Locate every Plasmodium falciparum parasite and identify its life-cycle stage.
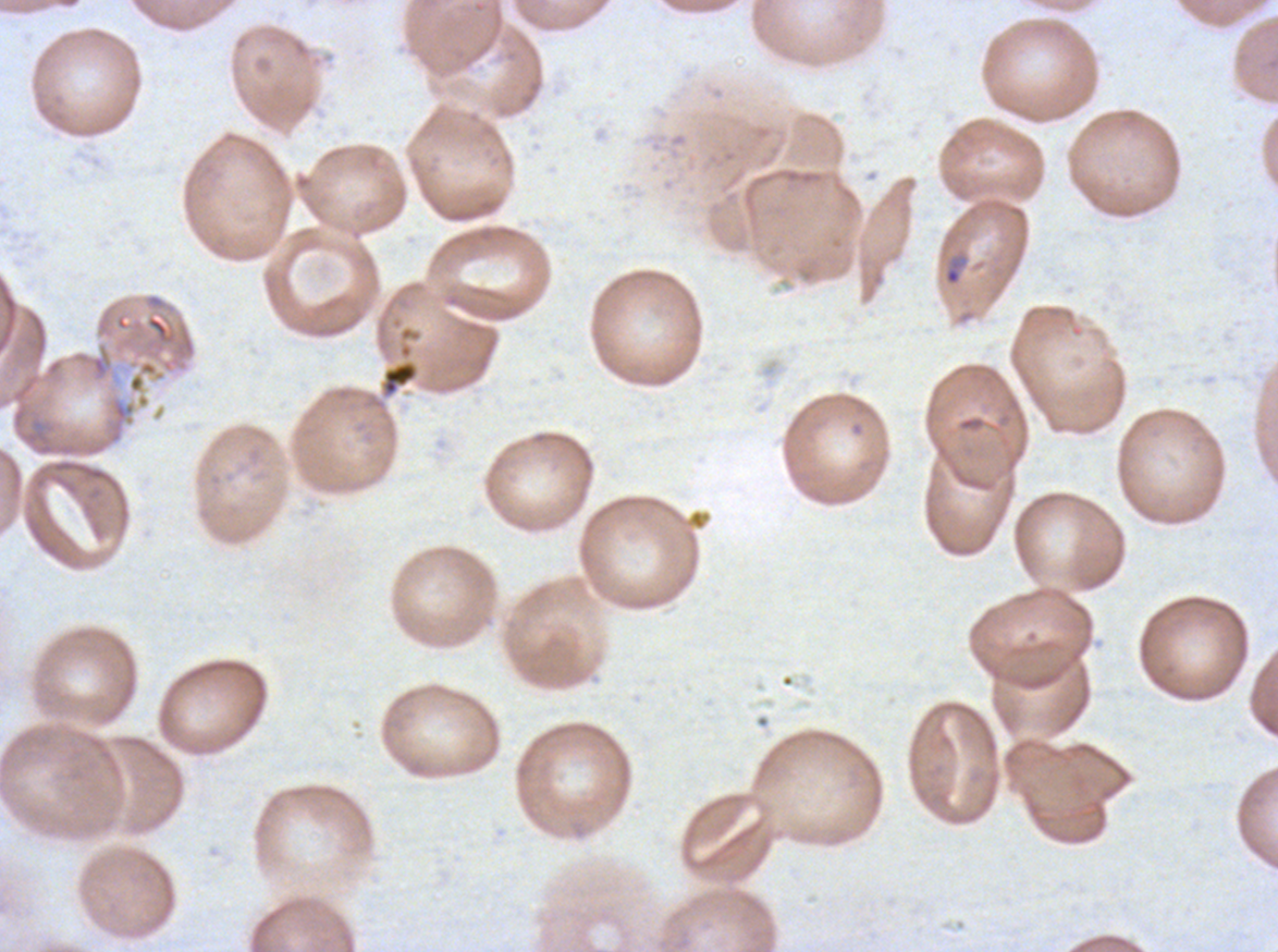

Approximate bounding rectangles given as corner coordinates in pixels from the top-left.
Rings: (x1=943, y1=254, x2=965, y2=287).
No late-ring/early-trophozoite forms, mid trophozoites, late trophozoites, early schizonts, late schizonts, segmenters, or gametocytes observed.

preparation: thin blood smear
debris_locations: 'approximate bounding rectangles given as corner coordinates in pixels from the top-left: (x1=380, y1=359, x2=419, y2=398), (x1=127, y1=360, x2=166, y2=394)'
image_size: 1278×952 pixels
specimen: Plasmodium falciparum cultured ex vivo for 24 to 48 hours, from a patient in The Gambia
stain: Giemsa
field_of_view: sub-image separated from a larger composite